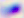 Toxoplasma gondii is seen. 400x magnification. Micrograph.